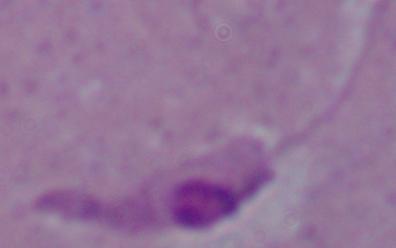

Summary:
  - Magnification: 1000x
  - Modality: micrograph
  - Identification: Leishmania